State the preparation type.
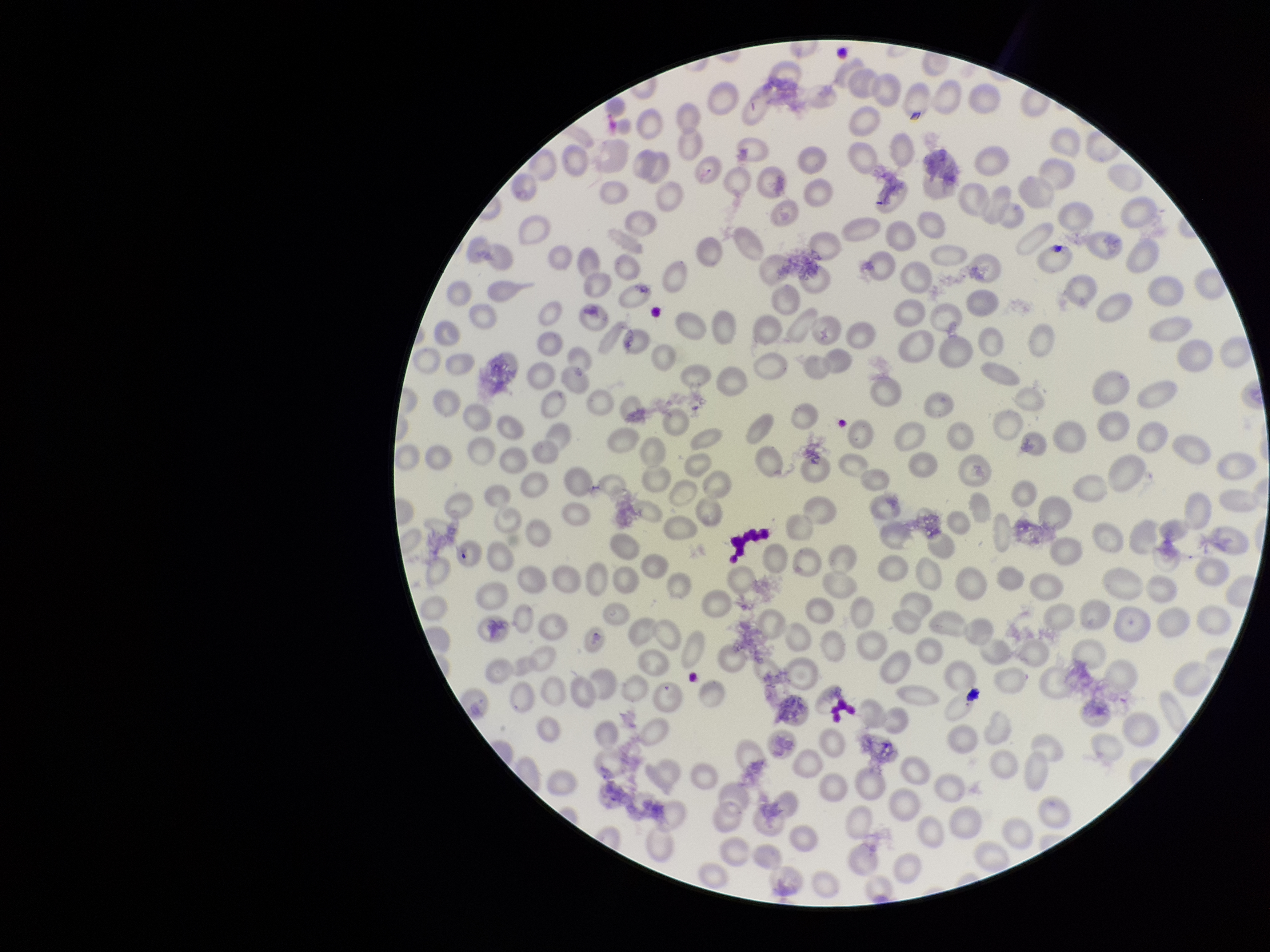

Thin.

{
  "red_blood_cell_count": 268,
  "patient_malaria_status": "negative",
  "capture": "smartphone photograph through the microscope eyepiece",
  "parasitized_red_blood_cells": "none detected",
  "field_of_view": "single",
  "image_size": "1270×952 pixels",
  "stain": "Giemsa",
  "parasitized_red_blood_cell_count": 0
}